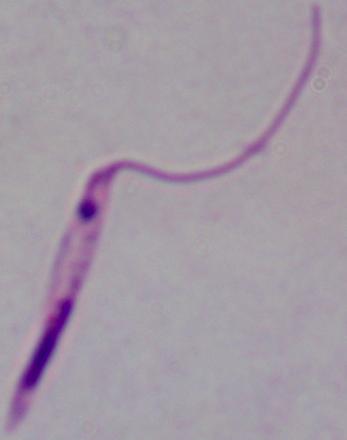
{
  "modality": "photomicrograph",
  "identification": "Leishmania",
  "magnification": "1000x"
}